Assess the morphology of the red blood cells.
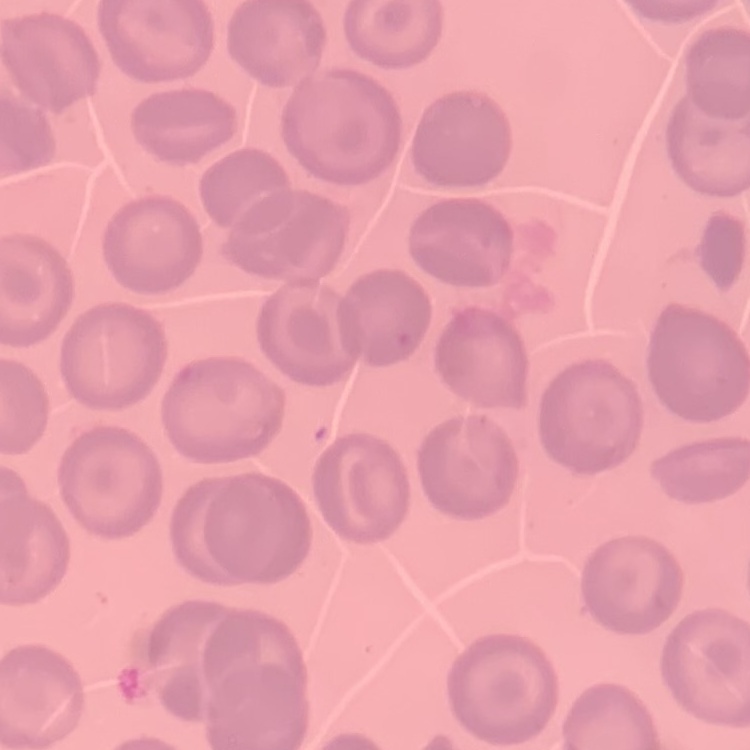
They show no rouleaux formation.

Thin blood film. Field's or Giemsa stain. One tile cut from a larger photomicrograph.